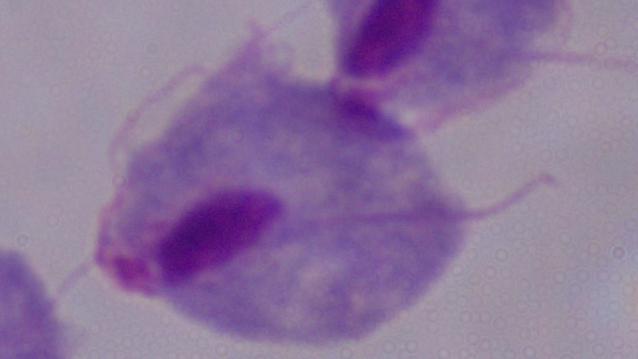

Photomicrograph. 1000x magnification. A trichomonad is shown.